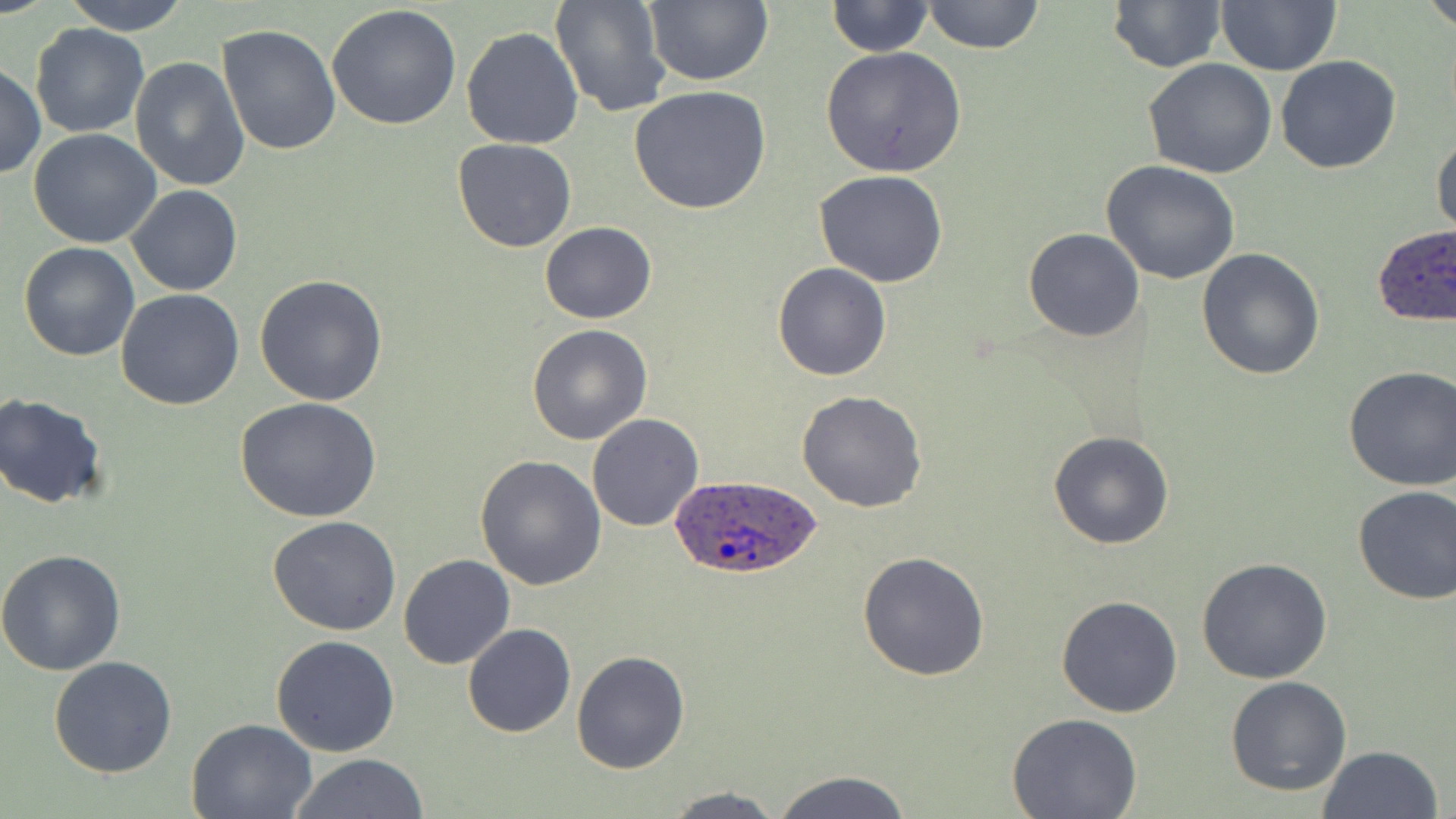
Summary:
  - Coordinate format: approximate bounding boxes as named x1/y1/x2/y2 corners in pixels
  - Uninfected red blood cell locations: (x1=59, y1=0, x2=195, y2=36), (x1=920, y1=0, x2=1044, y2=54), (x1=1107, y1=0, x2=1227, y2=72), (x1=1423, y1=0, x2=1456, y2=34), (x1=551, y1=1, x2=670, y2=118), (x1=825, y1=1, x2=933, y2=57), (x1=1216, y1=1, x2=1342, y2=75), (x1=642, y1=2, x2=773, y2=87), (x1=327, y1=5, x2=462, y2=131), (x1=29, y1=24, x2=148, y2=137), (x1=217, y1=25, x2=340, y2=156), (x1=461, y1=26, x2=583, y2=149), (x1=822, y1=46, x2=967, y2=177), (x1=1276, y1=55, x2=1401, y2=174), (x1=129, y1=56, x2=249, y2=192), (x1=1143, y1=59, x2=1277, y2=179), (x1=0, y1=63, x2=45, y2=180), (x1=628, y1=85, x2=773, y2=214), (x1=28, y1=128, x2=162, y2=248), (x1=1432, y1=130, x2=1456, y2=241), (x1=452, y1=138, x2=578, y2=253), (x1=1101, y1=161, x2=1242, y2=285), (x1=814, y1=170, x2=949, y2=288), (x1=128, y1=185, x2=242, y2=296), (x1=540, y1=220, x2=656, y2=324), (x1=1024, y1=228, x2=1145, y2=342), (x1=19, y1=243, x2=141, y2=363), (x1=1197, y1=247, x2=1327, y2=380), (x1=772, y1=263, x2=892, y2=381), (x1=255, y1=274, x2=387, y2=407), (x1=114, y1=289, x2=244, y2=410), (x1=527, y1=324, x2=653, y2=445), (x1=1343, y1=364, x2=1456, y2=492), (x1=796, y1=390, x2=927, y2=513), (x1=0, y1=392, x2=110, y2=509), (x1=234, y1=396, x2=383, y2=523), (x1=587, y1=413, x2=703, y2=532), (x1=1048, y1=429, x2=1176, y2=549), (x1=475, y1=456, x2=606, y2=591), (x1=1351, y1=485, x2=1456, y2=606), (x1=267, y1=516, x2=402, y2=637), (x1=0, y1=550, x2=128, y2=675), (x1=857, y1=551, x2=989, y2=682), (x1=398, y1=553, x2=515, y2=670), (x1=1196, y1=558, x2=1333, y2=684), (x1=1056, y1=595, x2=1184, y2=718), (x1=462, y1=623, x2=575, y2=737), (x1=272, y1=634, x2=400, y2=757), (x1=571, y1=649, x2=690, y2=773), (x1=48, y1=655, x2=177, y2=778), (x1=1225, y1=676, x2=1351, y2=796), (x1=1008, y1=713, x2=1142, y2=819), (x1=185, y1=717, x2=316, y2=819), (x1=1316, y1=746, x2=1443, y2=819), (x1=288, y1=753, x2=431, y2=818), (x1=770, y1=769, x2=915, y2=819), (x1=661, y1=787, x2=792, y2=818)
  - Plasmodium ovale-infected red blood cell locations: (x1=1373, y1=227, x2=1456, y2=330), (x1=667, y1=474, x2=822, y2=583)
  - Slide-level diagnosis: Plasmodium ovale
  - Modality: optical microscopy
  - Magnification: 1000x
  - Stain: May-Grünwald-Giemsa
  - Preparation: thin blood film
  - Image size: 1456×819 pixels
  - Field of view: one of a larger specimen